Classify this cell by malaria status.
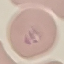

Parasitized.

Summary:
  - Preparation: thin smear
  - Image type: cell patch, automatically extracted from a larger field of view and resized to 64 × 64 pixels
  - Stain: Giemsa
  - Capture: smartphone through the microscope eyepiece